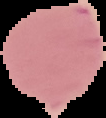

Summary:
  - Preparation: thin blood smear
  - Result: no malaria parasites detected
  - Image type: segmented cell region on a black background
  - Image size: 106×118 pixels